State which parasite is depicted.
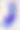
This is Toxoplasma gondii.

Micrograph. Captured at 400x magnification.